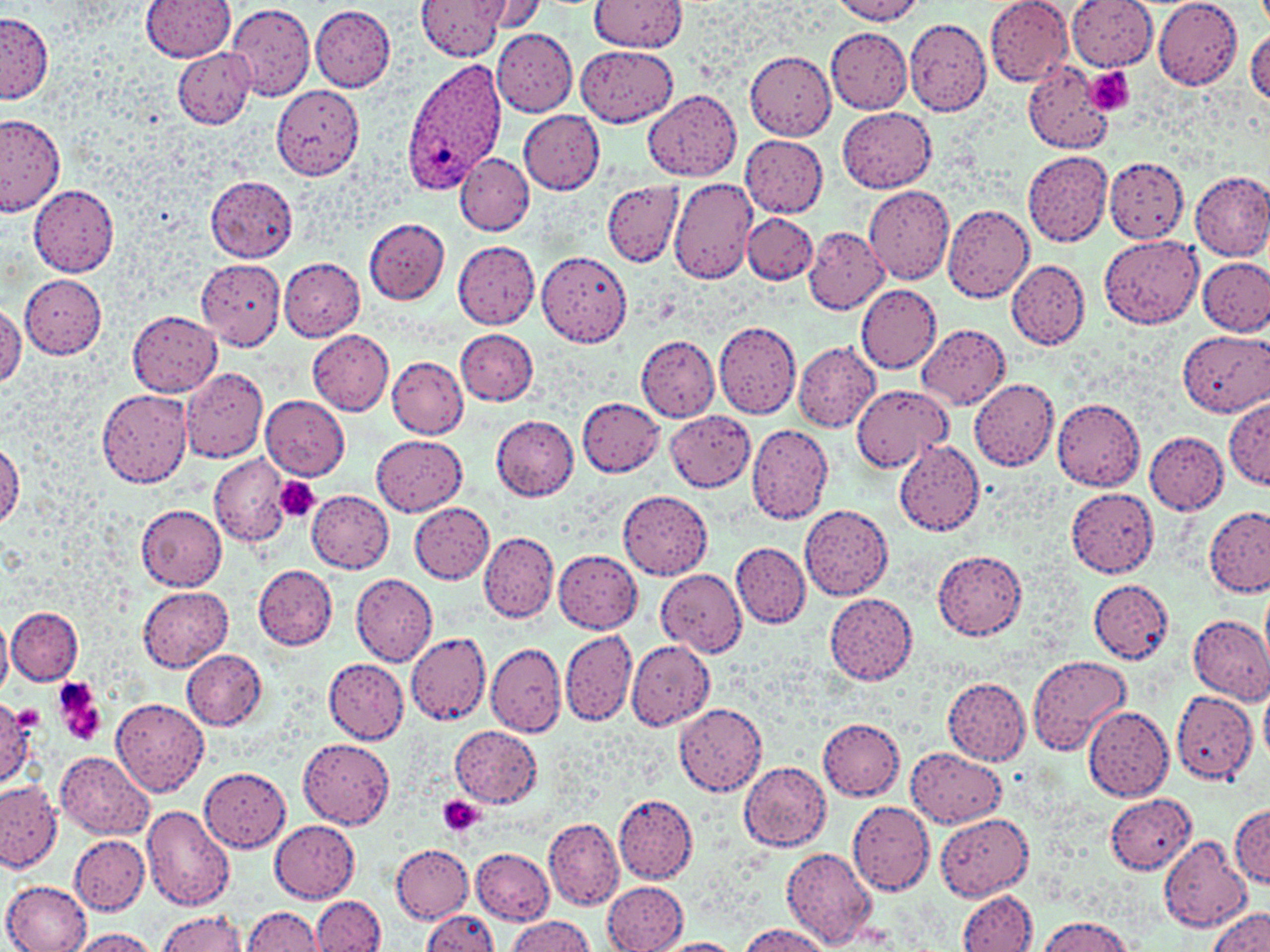
slide_level_diagnosis: Plasmodium ovale
image_size: 1270×952 pixels
preparation: thin blood film
magnification: 1000x
uninfected_red_blood_cell_locations: 'approximate bounding boxes as [x1, y1, x2, y2] in pixels: [419, 0, 508, 59], [478, 0, 549, 34], [831, 0, 925, 24], [985, 0, 1073, 86], [1066, 0, 1157, 72], [1154, 0, 1243, 90], [140, 1, 235, 60], [296, 1, 471, 81], [588, 1, 688, 52], [222, 4, 315, 101], [311, 5, 396, 92], [1, 12, 53, 104], [904, 18, 991, 115], [826, 27, 913, 112], [1246, 27, 1270, 106], [492, 29, 578, 116], [576, 44, 678, 127], [172, 47, 256, 129], [744, 51, 837, 139], [1024, 62, 1114, 154], [271, 85, 365, 180], [644, 90, 741, 180], [837, 107, 936, 192], [518, 109, 605, 194], [0, 112, 66, 217], [741, 135, 828, 217], [1023, 150, 1113, 246], [456, 154, 532, 235], [1105, 157, 1190, 242], [1190, 171, 1270, 260], [206, 177, 297, 261], [671, 177, 759, 283], [604, 182, 684, 265], [864, 184, 955, 284], [29, 185, 118, 274], [941, 206, 1034, 303], [742, 214, 816, 285], [364, 218, 450, 304], [803, 228, 888, 313], [1100, 234, 1204, 327], [453, 241, 541, 329], [536, 251, 632, 348], [279, 256, 365, 341], [1198, 256, 1270, 336], [197, 260, 285, 350], [1008, 261, 1089, 350], [20, 274, 107, 357], [856, 284, 942, 374], [0, 304, 24, 387], [128, 312, 221, 395], [714, 320, 802, 419], [918, 324, 1009, 408], [456, 329, 538, 406], [1179, 329, 1270, 418], [308, 330, 394, 415], [635, 333, 719, 421], [794, 342, 880, 431], [387, 358, 467, 438], [180, 367, 267, 463], [969, 378, 1059, 471], [849, 385, 954, 472], [97, 389, 193, 488], [260, 395, 350, 479], [577, 397, 665, 477], [1223, 397, 1270, 489], [1052, 400, 1146, 489], [665, 411, 755, 491], [491, 414, 579, 501], [746, 424, 833, 525], [1145, 432, 1228, 514], [372, 434, 467, 514], [0, 439, 22, 530], [895, 439, 985, 535], [210, 455, 292, 547], [1066, 488, 1159, 577], [307, 490, 394, 573], [617, 490, 712, 579], [409, 502, 495, 582], [799, 503, 893, 600], [137, 505, 227, 590], [1206, 506, 1270, 597], [480, 532, 558, 622], [730, 542, 810, 628], [554, 550, 641, 634], [933, 550, 1027, 640], [253, 565, 338, 649], [657, 569, 747, 656], [352, 575, 436, 665], [1088, 580, 1172, 664], [138, 587, 232, 670], [824, 593, 917, 684], [6, 607, 83, 685], [0, 614, 14, 698], [1188, 614, 1270, 702], [561, 630, 637, 726], [408, 635, 492, 729], [627, 640, 714, 731], [486, 643, 566, 737], [182, 649, 267, 731], [1026, 655, 1131, 756], [323, 658, 408, 742], [944, 678, 1031, 765], [1261, 685, 1270, 766], [1171, 688, 1259, 786], [1, 699, 39, 787], [111, 699, 209, 797], [674, 703, 766, 796], [1083, 707, 1174, 802], [818, 718, 906, 800], [451, 726, 541, 807], [299, 738, 393, 829], [907, 746, 1005, 828], [55, 750, 154, 841], [739, 759, 833, 851], [198, 765, 290, 852], [0, 780, 62, 873], [613, 792, 698, 883], [1105, 794, 1197, 873], [849, 802, 935, 895], [141, 803, 235, 911], [1231, 803, 1269, 887], [935, 812, 1034, 900], [543, 816, 624, 910], [270, 820, 360, 902], [70, 834, 149, 915], [1159, 838, 1249, 930], [391, 843, 473, 922], [473, 848, 555, 925], [783, 848, 876, 948], [3, 879, 90, 952], [602, 880, 687, 951], [959, 889, 1037, 951], [312, 895, 385, 952], [241, 906, 325, 952], [424, 908, 497, 951], [1206, 909, 1270, 952], [156, 910, 247, 952], [506, 916, 596, 952], [1038, 916, 1135, 951], [739, 925, 831, 952], [66, 928, 161, 952], [656, 938, 743, 952]'
platelet_locations: 'approximate bounding boxes as [x1, y1, x2, y2] in pixels: [1087, 67, 1134, 115], [275, 476, 319, 522], [56, 690, 107, 748], [438, 795, 483, 837]'
plasmodium_ovale_infected_red_blood_cell_locations: 'approximate bounding boxes as [x1, y1, x2, y2] in pixels: [401, 57, 508, 194]'
stain: May-Grünwald-Giemsa
modality: optical microscopy
field_of_view: one of a larger specimen